State the blood parasite species.
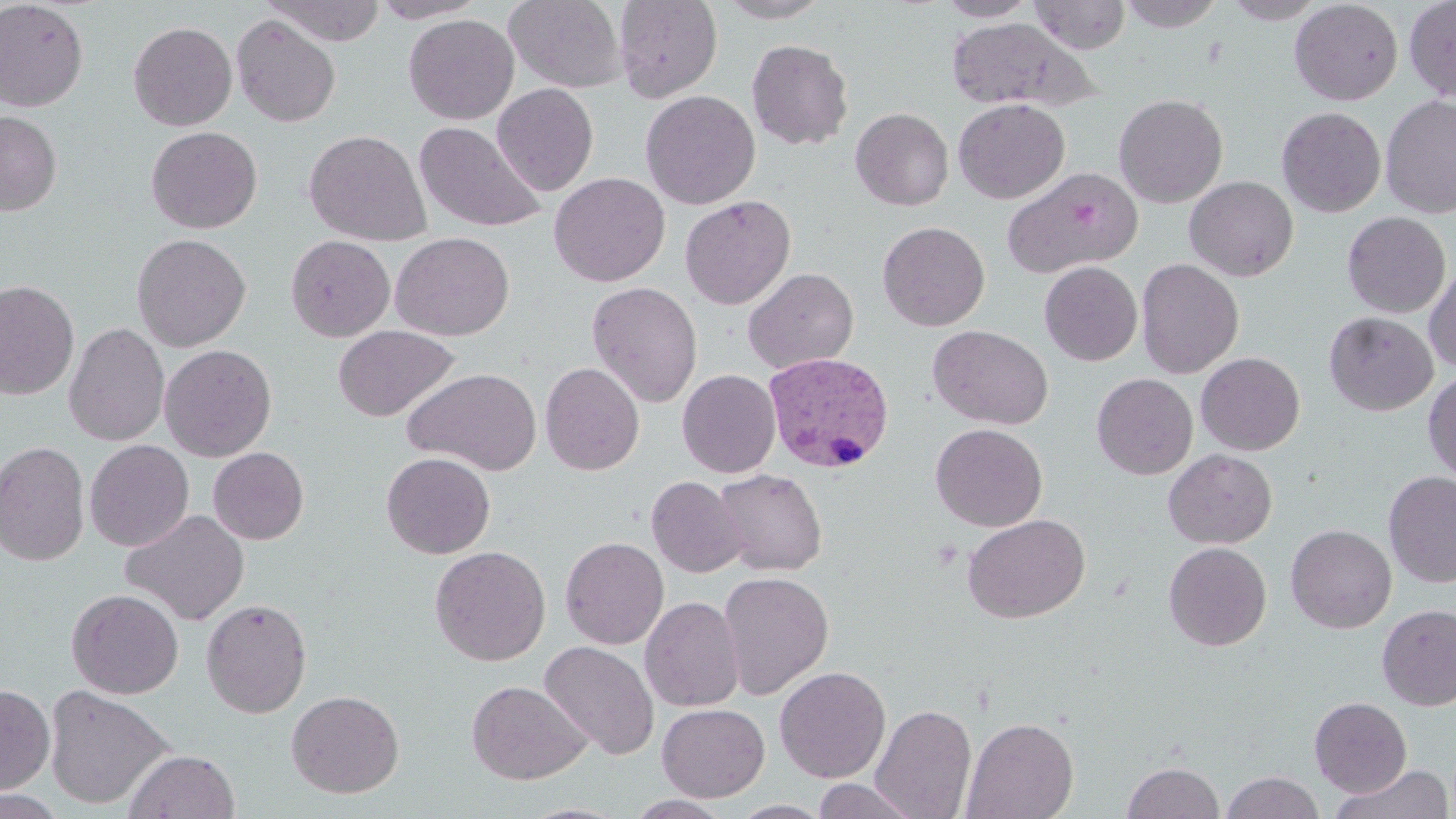
Plasmodium vivax.

uninfected red blood cell locations = approximate bounding boxes as named x1/y1/x2/y2 corners in pixels: (x1=264, y1=0, x2=386, y2=45), (x1=370, y1=0, x2=486, y2=23), (x1=504, y1=0, x2=628, y2=94), (x1=613, y1=0, x2=722, y2=102), (x1=714, y1=0, x2=832, y2=23), (x1=935, y1=0, x2=1038, y2=21), (x1=1029, y1=0, x2=1131, y2=54), (x1=1221, y1=0, x2=1328, y2=23), (x1=1404, y1=0, x2=1456, y2=103), (x1=0, y1=1, x2=89, y2=111), (x1=1117, y1=1, x2=1226, y2=31), (x1=1289, y1=1, x2=1403, y2=105), (x1=231, y1=14, x2=341, y2=127), (x1=403, y1=14, x2=519, y2=124), (x1=946, y1=17, x2=1094, y2=111), (x1=128, y1=21, x2=238, y2=131), (x1=746, y1=39, x2=854, y2=150), (x1=492, y1=83, x2=598, y2=195), (x1=640, y1=90, x2=760, y2=210), (x1=1113, y1=94, x2=1228, y2=208), (x1=1380, y1=95, x2=1456, y2=218), (x1=953, y1=98, x2=1069, y2=203), (x1=1277, y1=106, x2=1386, y2=217), (x1=850, y1=107, x2=953, y2=211), (x1=0, y1=110, x2=61, y2=216), (x1=414, y1=121, x2=546, y2=232), (x1=146, y1=126, x2=262, y2=233), (x1=304, y1=129, x2=431, y2=246), (x1=1003, y1=167, x2=1142, y2=278), (x1=549, y1=172, x2=670, y2=286), (x1=1185, y1=176, x2=1299, y2=281), (x1=679, y1=195, x2=796, y2=309), (x1=1341, y1=211, x2=1451, y2=318), (x1=878, y1=221, x2=990, y2=331), (x1=391, y1=232, x2=514, y2=340), (x1=131, y1=233, x2=251, y2=352), (x1=285, y1=235, x2=395, y2=341), (x1=1136, y1=259, x2=1244, y2=378), (x1=1039, y1=261, x2=1143, y2=366), (x1=1423, y1=261, x2=1456, y2=373), (x1=742, y1=267, x2=859, y2=374), (x1=0, y1=280, x2=79, y2=400), (x1=587, y1=281, x2=702, y2=406), (x1=1323, y1=311, x2=1438, y2=416), (x1=64, y1=323, x2=170, y2=446), (x1=333, y1=325, x2=459, y2=421), (x1=927, y1=325, x2=1053, y2=430), (x1=159, y1=344, x2=277, y2=461), (x1=1196, y1=352, x2=1305, y2=455), (x1=540, y1=362, x2=644, y2=475), (x1=401, y1=367, x2=541, y2=475), (x1=677, y1=369, x2=781, y2=477), (x1=1422, y1=371, x2=1456, y2=484), (x1=1092, y1=373, x2=1199, y2=479), (x1=930, y1=423, x2=1047, y2=531), (x1=0, y1=440, x2=89, y2=566), (x1=85, y1=440, x2=194, y2=551), (x1=208, y1=447, x2=309, y2=544), (x1=1163, y1=449, x2=1277, y2=548), (x1=381, y1=452, x2=496, y2=558), (x1=713, y1=468, x2=827, y2=576), (x1=1383, y1=471, x2=1456, y2=588), (x1=646, y1=476, x2=748, y2=578), (x1=120, y1=509, x2=249, y2=626), (x1=962, y1=514, x2=1090, y2=623), (x1=1285, y1=524, x2=1397, y2=633), (x1=560, y1=536, x2=669, y2=649), (x1=1163, y1=542, x2=1271, y2=651), (x1=429, y1=545, x2=551, y2=666), (x1=718, y1=570, x2=834, y2=699), (x1=66, y1=589, x2=184, y2=698), (x1=640, y1=596, x2=744, y2=711), (x1=201, y1=598, x2=312, y2=718), (x1=1376, y1=603, x2=1456, y2=711), (x1=539, y1=641, x2=659, y2=760), (x1=774, y1=666, x2=891, y2=782), (x1=466, y1=680, x2=591, y2=785), (x1=0, y1=683, x2=55, y2=795), (x1=44, y1=684, x2=176, y2=809), (x1=286, y1=690, x2=405, y2=798), (x1=1309, y1=697, x2=1412, y2=797), (x1=657, y1=703, x2=769, y2=802), (x1=871, y1=704, x2=977, y2=819), (x1=962, y1=717, x2=1079, y2=819), (x1=123, y1=749, x2=240, y2=818), (x1=1122, y1=760, x2=1225, y2=819), (x1=1329, y1=763, x2=1454, y2=819), (x1=1222, y1=771, x2=1325, y2=819), (x1=811, y1=778, x2=923, y2=818), (x1=0, y1=789, x2=68, y2=819), (x1=626, y1=795, x2=735, y2=818), (x1=728, y1=801, x2=833, y2=818)
image size = 1456×819 pixels
magnification = 1000x
stain = May-Grünwald-Giemsa
modality = optical microscopy
Plasmodium vivax-infected red blood cell locations = approximate bounding boxes as named x1/y1/x2/y2 corners in pixels: (x1=762, y1=351, x2=894, y2=473)
field of view = single
preparation = thin blood film